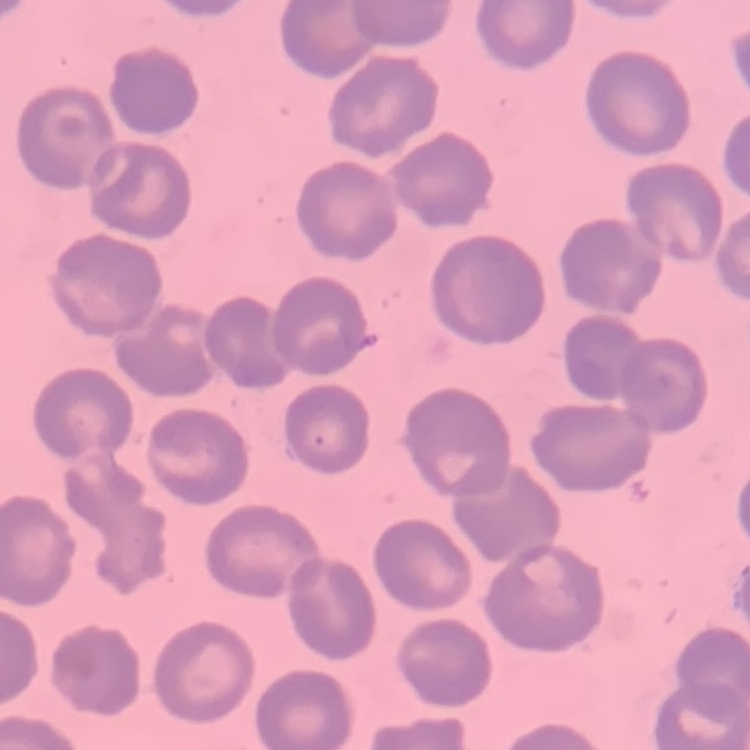

The erythrocytes show no rouleaux formation. Field's or Giemsa stain. One tile cut from a larger photomicrograph. Thin blood smear.